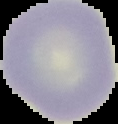

image size = 118×124 pixels
image type = segmented cell region on a black background
preparation = thin blood film
malaria status = uninfected